Locate every Plasmodium falciparum-infected red blood cell.
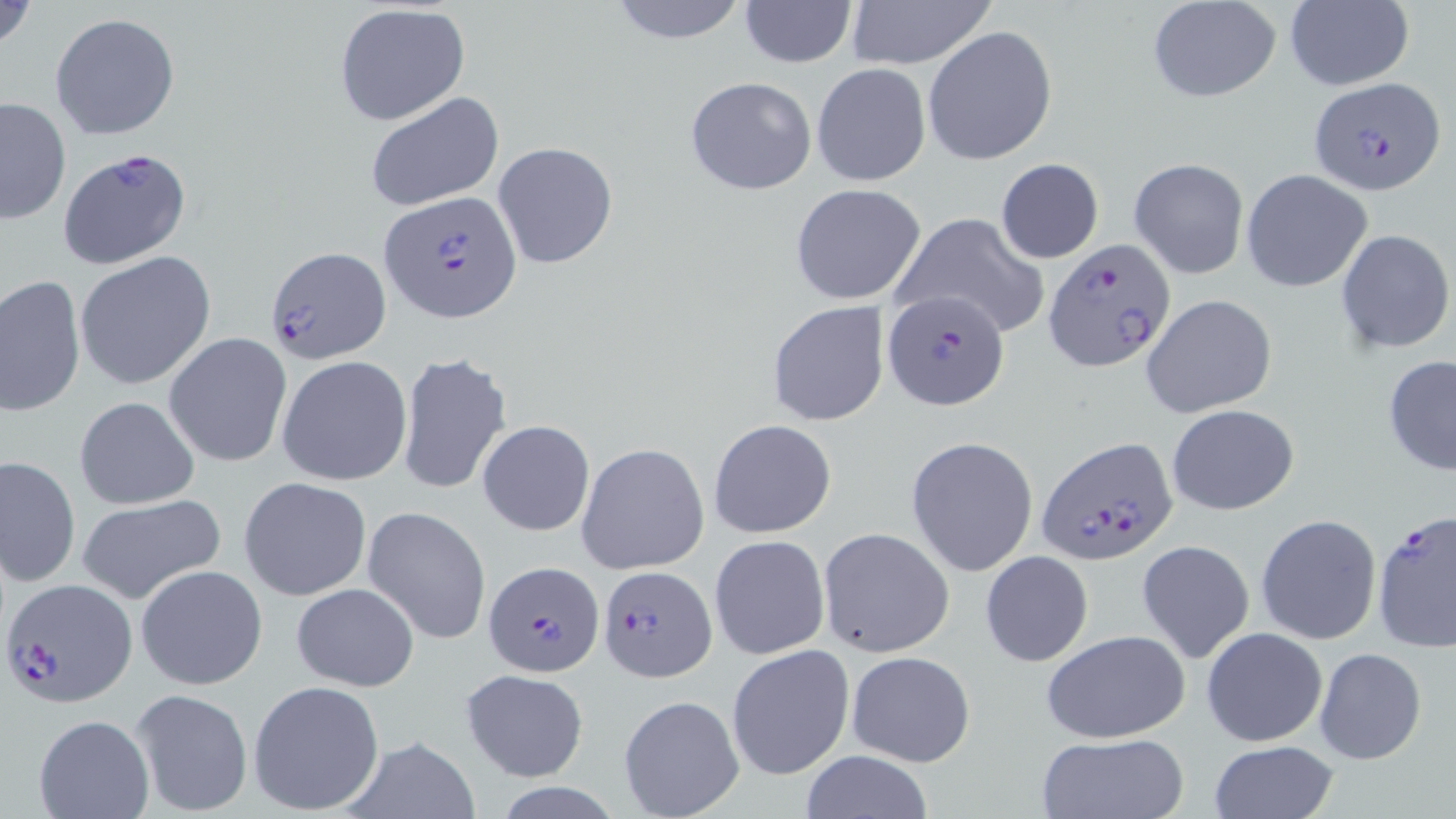

Approximate bounding boxes as [x1, y1, x2, y2] in pixels.
Plasmodium falciparum-infected red blood cells: [1308, 76, 1444, 195], [58, 149, 192, 270], [381, 192, 522, 321], [1044, 240, 1175, 372], [264, 246, 392, 364], [883, 289, 1009, 412], [1037, 435, 1175, 565], [1373, 510, 1456, 652], [483, 559, 605, 678], [598, 564, 714, 681], [4, 579, 137, 706].

Uninfected red blood cell locations: [1, 0, 40, 57], [605, 0, 750, 45], [844, 0, 996, 70], [738, 1, 857, 68], [1148, 1, 1281, 102], [1281, 2, 1414, 90], [334, 4, 470, 126], [50, 12, 181, 139], [923, 25, 1057, 165], [812, 63, 931, 187], [685, 76, 817, 196], [364, 91, 504, 211], [1, 96, 71, 225], [491, 142, 618, 268], [1129, 158, 1249, 279], [996, 159, 1104, 264], [1240, 167, 1374, 292], [790, 183, 927, 306], [891, 213, 1048, 338], [1336, 229, 1454, 354], [75, 251, 217, 390], [0, 274, 86, 418], [1141, 294, 1277, 418], [767, 301, 889, 426], [163, 332, 292, 468], [396, 352, 512, 495], [278, 355, 412, 486], [1382, 356, 1456, 476], [75, 395, 201, 510], [1166, 403, 1299, 515], [708, 418, 837, 538], [477, 420, 595, 536], [906, 436, 1039, 576], [577, 442, 710, 574], [1, 456, 80, 587], [239, 477, 371, 601], [76, 492, 225, 605], [364, 507, 492, 643], [1255, 513, 1382, 645], [818, 528, 954, 658], [709, 534, 830, 661], [1136, 539, 1256, 665], [980, 550, 1094, 668], [136, 564, 267, 690], [290, 582, 419, 691], [1202, 627, 1329, 746], [1041, 630, 1192, 743], [725, 644, 855, 780], [1315, 648, 1427, 764], [846, 650, 976, 767], [460, 669, 587, 781], [248, 681, 385, 813], [131, 687, 253, 816], [617, 694, 744, 818], [35, 715, 153, 819], [1036, 732, 1189, 818], [340, 735, 481, 818], [1206, 741, 1343, 819], [797, 750, 934, 819]. Slide-level diagnosis: Plasmodium falciparum. Single field of view. May-Grünwald-Giemsa-stained preparation. Thin blood film. Light microscopy. 1000x magnification. Image is 1456×819 pixels.